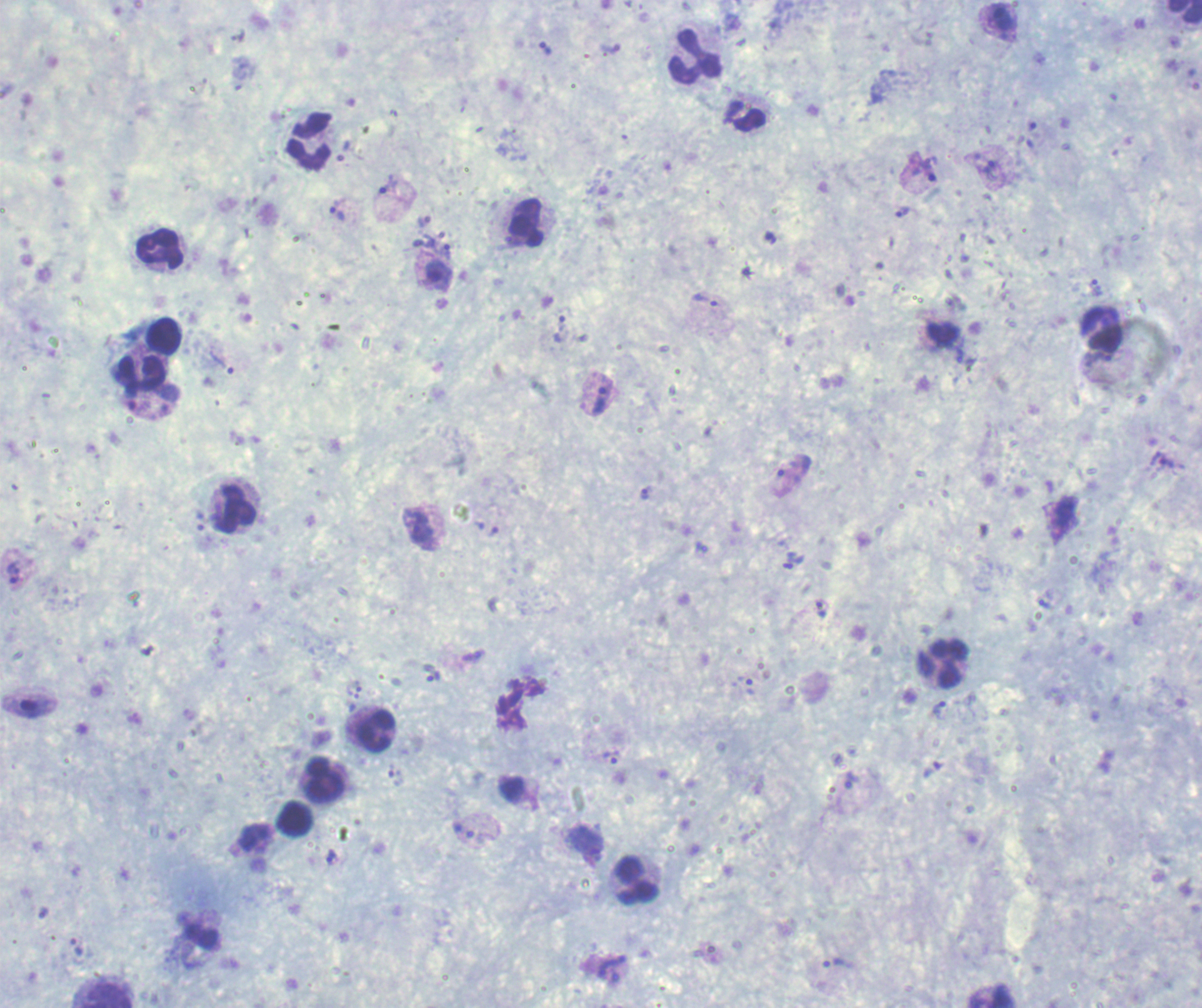
Approximate centers as [x, y] in pixels.
Summary:
  - Leukocyte locations: [1184, 12], [695, 55], [746, 116], [309, 141], [526, 223], [161, 249], [1101, 329], [164, 336], [141, 372], [234, 509], [942, 663], [377, 732], [324, 780], [296, 819], [638, 881], [103, 995]
  - Trophozoite locations: [238, 35], [545, 49], [610, 49], [241, 79], [1032, 126], [344, 151], [990, 169], [924, 170], [385, 186], [336, 210], [902, 211], [425, 221], [424, 241], [446, 252], [438, 275], [1097, 288], [709, 303], [562, 326], [222, 363], [596, 395], [131, 404], [1163, 462], [791, 475], [646, 492], [198, 518], [479, 525], [421, 529], [493, 531], [794, 561], [14, 572], [1045, 605], [821, 609], [473, 657], [431, 672], [743, 683], [354, 690], [939, 711], [611, 758], [395, 777], [851, 780], [469, 833], [586, 846], [332, 856], [76, 947], [837, 964], [611, 970]
  - Result: malaria parasites identified
  - Magnification: 100x
  - Preparation: thick blood film
  - Stain: Romanowsky
  - Background quality: good
  - Field of view: one from this slide
  - Context: previously used in an actual diagnosis
  - Image size: 1202×1008 pixels